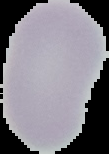

Summary:
  - Image size: 109×154 pixels
  - Malaria status: uninfected
  - Preparation: thin blood film
  - Image type: segmented cell region with the area outside set to black